Outline each uninfected red blood cell.
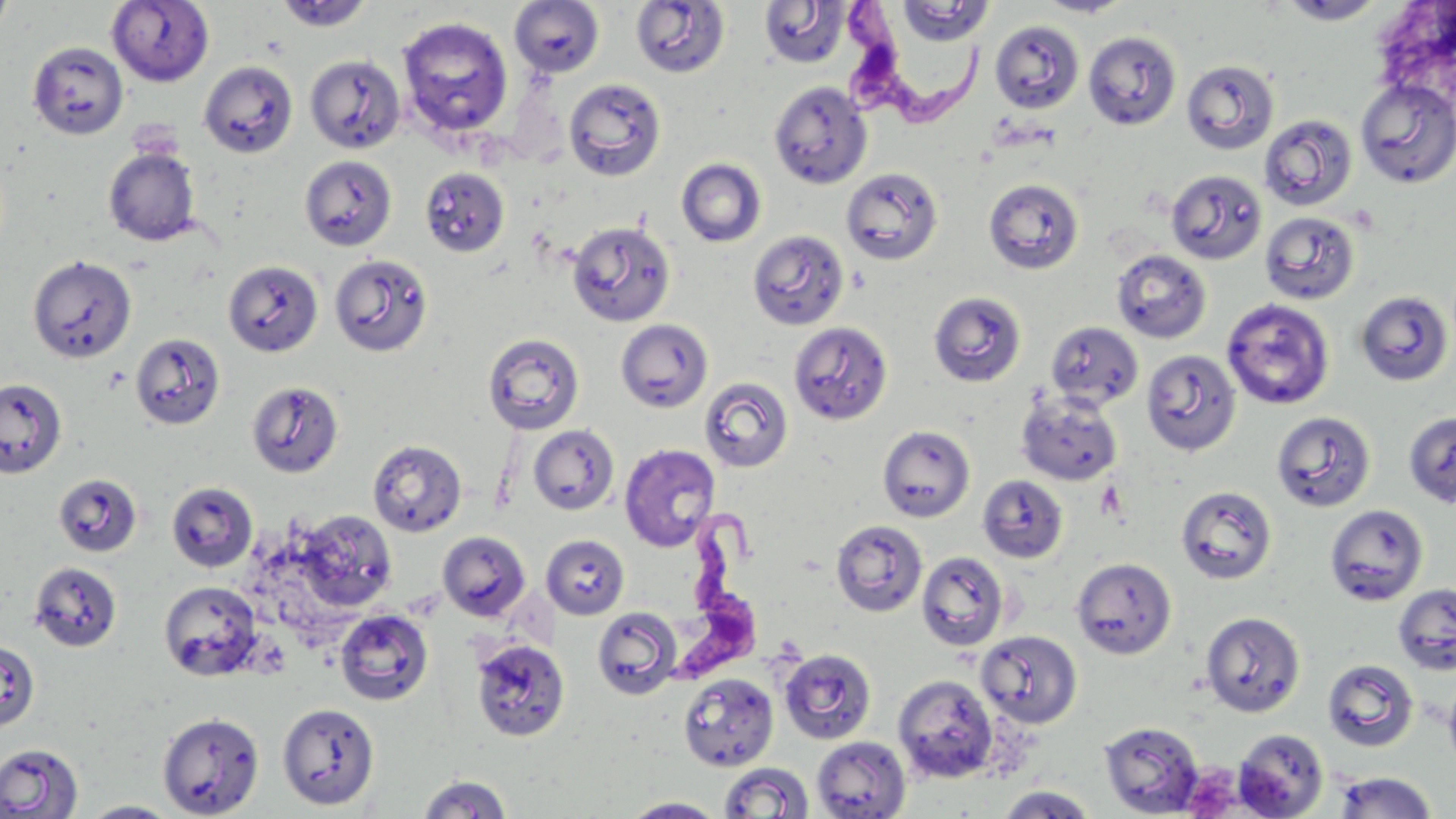

Approximate bounding boxes as (x1, y1, x2, y2) in pixels.
Uninfected red blood cells: (107, 0, 214, 86), (275, 0, 374, 32), (1039, 0, 1132, 17), (1277, 0, 1387, 24), (0, 1, 16, 44), (509, 1, 605, 78), (630, 1, 729, 78), (759, 1, 851, 69), (896, 1, 994, 45), (397, 17, 514, 139), (989, 20, 1085, 114), (1084, 31, 1181, 130), (27, 41, 128, 140), (304, 54, 406, 154), (1182, 59, 1280, 155), (198, 61, 298, 158), (564, 78, 666, 182), (1355, 78, 1456, 189), (769, 80, 873, 189), (1258, 115, 1358, 211), (103, 146, 201, 247), (299, 155, 398, 251), (676, 158, 767, 247), (419, 167, 511, 257), (841, 167, 944, 265), (1166, 169, 1267, 265), (984, 178, 1084, 274), (1260, 211, 1360, 305), (566, 220, 675, 327), (748, 230, 850, 330), (1112, 249, 1212, 344), (329, 253, 433, 357), (28, 255, 137, 364), (223, 260, 323, 357), (928, 291, 1026, 387), (1355, 291, 1453, 386), (1221, 298, 1335, 409), (615, 318, 714, 413), (1046, 320, 1143, 410), (788, 321, 893, 425), (130, 332, 226, 430), (482, 333, 585, 435), (1141, 350, 1241, 456), (699, 377, 794, 472), (0, 378, 67, 478), (246, 381, 344, 478), (1017, 391, 1123, 486), (1271, 411, 1376, 512), (1403, 411, 1456, 508), (528, 425, 620, 515), (877, 425, 975, 522), (367, 438, 467, 537), (619, 443, 721, 552), (53, 473, 142, 557), (978, 475, 1069, 563), (166, 481, 259, 573), (1176, 485, 1277, 585), (1324, 504, 1429, 606), (292, 509, 398, 613), (831, 519, 927, 617), (437, 531, 531, 622), (542, 534, 630, 619), (916, 551, 1010, 651), (1070, 557, 1177, 659), (29, 561, 122, 652), (158, 579, 264, 681), (1393, 582, 1456, 676), (592, 607, 683, 700), (334, 608, 434, 705), (1200, 611, 1305, 717), (976, 630, 1083, 728), (470, 638, 570, 743), (0, 641, 40, 732), (779, 648, 877, 745), (1322, 658, 1420, 753), (678, 673, 778, 771), (892, 674, 999, 783), (1443, 678, 1456, 772), (277, 702, 380, 810), (157, 712, 264, 818), (1099, 721, 1205, 817), (1233, 728, 1329, 819), (811, 736, 911, 819), (0, 744, 83, 818), (718, 762, 815, 818), (1334, 772, 1437, 818), (416, 774, 513, 817), (996, 785, 1099, 818), (620, 797, 726, 818), (78, 801, 182, 818).

Summary:
  - Platelet locations: (1094, 479, 1128, 522)
  - Trypanosoma brucei locations: (833, 0, 988, 131), (665, 505, 770, 695)
  - Slide-level diagnosis: Trypanosoma brucei
  - Magnification: 1000x
  - Field of view: single
  - Stain: May-Grünwald-Giemsa
  - Modality: optical microscopy
  - Preparation: thin blood smear
  - Image size: 1456×819 pixels